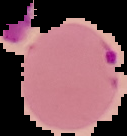

Summary:
  - Malaria status: parasitized
  - Image size: 127×136 pixels
  - Preparation: thin blood film
  - Image type: segmented cell region with the area outside set to black